Locate the red blood cells and classify each one as P. falciparum-infected, uninfected, or of indeterminate infection status.
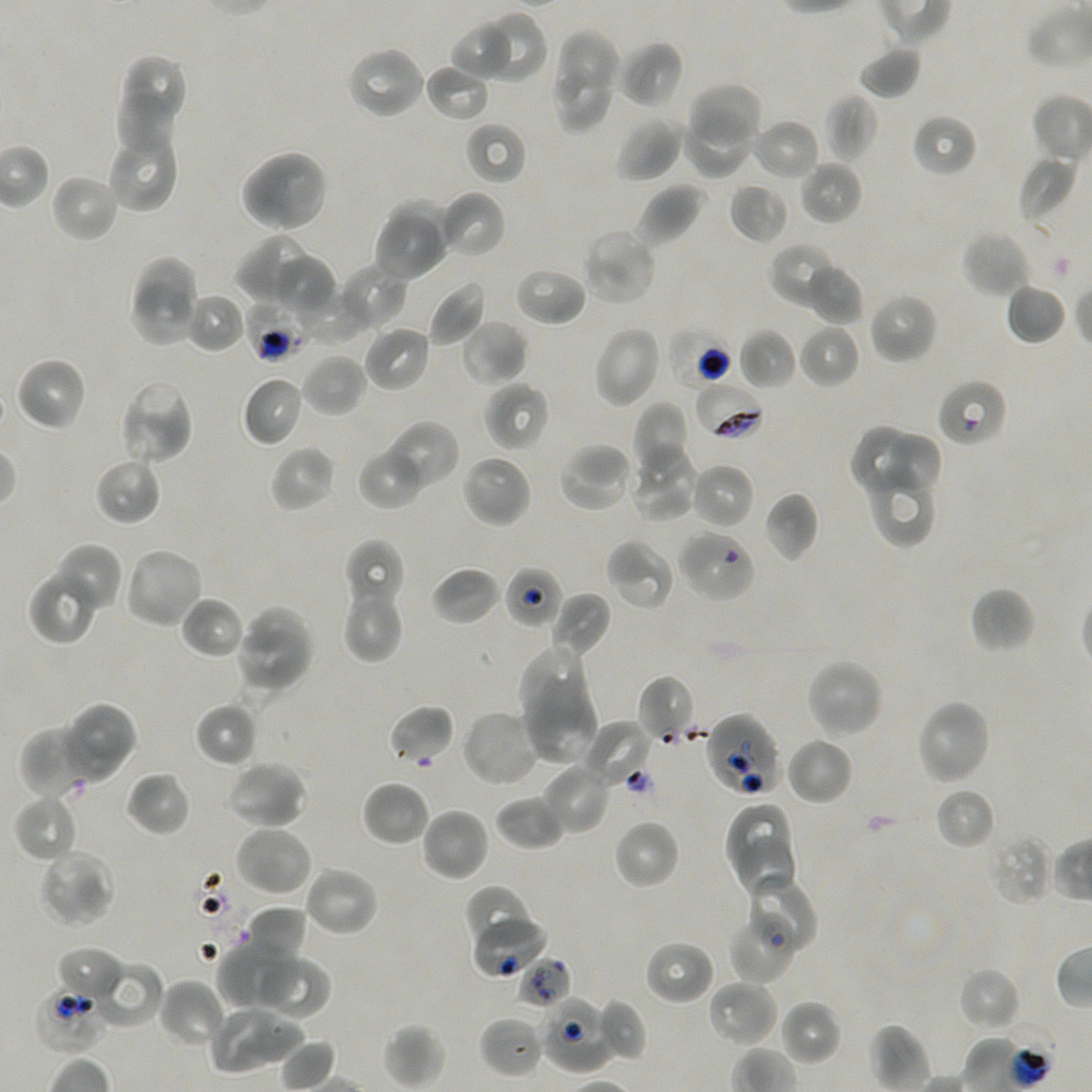
Approximate bounding boxes as {x1, y1, x2, y2} in pixels. Not every red blood cell is marked.
Infected red blood cells: {697, 382, 765, 437}.
Red blood cells of indeterminate infection status: {244, 298, 311, 363}, {666, 326, 733, 390}, {941, 382, 1005, 444}, {503, 564, 564, 630}, {704, 712, 783, 798}, {472, 911, 548, 979}, {731, 919, 794, 985}, {515, 956, 572, 1010}, {34, 984, 106, 1054}, {539, 996, 615, 1074}.
Uninfected red blood cells: {481, 10, 547, 81}, {452, 26, 511, 75}, {558, 30, 619, 91}, {617, 40, 684, 109}, {858, 45, 923, 100}, {344, 46, 426, 120}, {125, 56, 187, 121}, {424, 63, 490, 122}, {554, 69, 615, 130}, {690, 83, 762, 147}, {114, 88, 180, 153}, {822, 93, 878, 162}, {683, 109, 754, 179}, {911, 113, 977, 178}, {615, 117, 685, 182}, {751, 118, 820, 181}, {464, 121, 527, 185}, {109, 133, 180, 213}, {239, 149, 329, 233}, {1018, 154, 1076, 224}, {798, 159, 862, 225}, {49, 173, 120, 243}, {729, 181, 788, 244}, {636, 183, 706, 248}, {437, 191, 506, 258}, {392, 200, 456, 266}, {373, 217, 448, 282}, {580, 228, 658, 306}, {962, 230, 1032, 299}, {235, 233, 316, 306}, {768, 242, 841, 308}, {274, 256, 336, 317}, {136, 257, 201, 319}, {336, 263, 407, 333}, {806, 263, 864, 325}, {513, 266, 587, 327}, {133, 280, 200, 347}, {426, 280, 486, 348}, {1005, 283, 1067, 345}, {297, 286, 370, 345}, {183, 292, 247, 354}, {867, 293, 939, 365}, {460, 319, 528, 386}, {798, 323, 859, 388}, {362, 325, 431, 393}, {593, 325, 662, 409}, {738, 328, 797, 390}, {301, 353, 367, 418}, {15, 356, 88, 431}, {242, 376, 306, 447}, {118, 380, 195, 466}, {484, 381, 550, 452}, {632, 401, 687, 469}, {382, 420, 460, 492}, {850, 425, 912, 491}, {888, 431, 943, 494}, {558, 442, 636, 514}, {629, 444, 699, 522}, {269, 445, 335, 513}, {358, 445, 426, 509}, {460, 453, 533, 529}, {94, 457, 162, 526}, {690, 462, 755, 530}, {871, 462, 932, 547}, {763, 492, 819, 563}, {677, 529, 757, 602}, {605, 538, 675, 610}, {344, 540, 404, 611}, {52, 542, 123, 614}, {122, 546, 205, 630}, {431, 566, 501, 626}, {27, 570, 98, 645}, {342, 584, 404, 663}, {969, 587, 1036, 653}, {551, 592, 612, 656}, {181, 596, 245, 658}, {243, 604, 314, 655}, {238, 625, 312, 687}, {517, 644, 587, 721}, {805, 657, 885, 740}, {638, 674, 698, 744}, {525, 683, 598, 765}, {915, 698, 992, 786}, {62, 702, 136, 782}, {194, 702, 258, 768}, {388, 704, 456, 765}, {460, 709, 542, 788}, {579, 721, 652, 787}, {20, 725, 101, 800}, {784, 735, 854, 806}, {225, 759, 308, 830}, {542, 763, 613, 836}, {125, 771, 192, 837}, {361, 780, 431, 847}, {934, 786, 995, 850}, {13, 793, 79, 862}, {495, 794, 567, 850}, {724, 803, 790, 873}, {420, 807, 490, 882}, {613, 818, 680, 890}, {234, 824, 314, 898}, {986, 831, 1053, 906}, {738, 837, 798, 898}, {38, 848, 115, 929}, {303, 865, 380, 938}, {750, 875, 818, 950}, {462, 884, 538, 951}, {244, 906, 308, 964}, {644, 939, 715, 1006}, {230, 941, 299, 1008}, {56, 945, 123, 1002}, {218, 945, 275, 1012}, {253, 954, 331, 1019}, {92, 960, 164, 1029}, {958, 966, 1022, 1032}, {158, 979, 226, 1048}, {706, 979, 778, 1048}, {595, 998, 648, 1063}, {779, 999, 841, 1066}, {208, 1004, 276, 1073}, {479, 1015, 545, 1078}, {255, 1022, 307, 1063}, {383, 1023, 445, 1089}.

{
  "culture": "in-vitro P. falciparum strain NF54, static",
  "field_of_view": "one from this slide",
  "donor_blood_group": "A+/O+",
  "objective": "100x, oil immersion, numerical aperture 1.45",
  "preparation": "thin blood smear",
  "stain": "Giemsa",
  "image_size": "1092×1092 pixels"
}